Assess this cell for malaria.
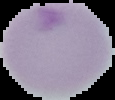
It is uninfected.

From a thin blood film. Image is 115×100 pixels. Cell region segmented out of the field of view; the surrounding area is masked to black.